Report the malaria status of this cell.
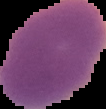

Uninfected.

image type = cell region segmented out of the field of view; surrounding area masked to black
preparation = thin blood film
image size = 106×109 pixels